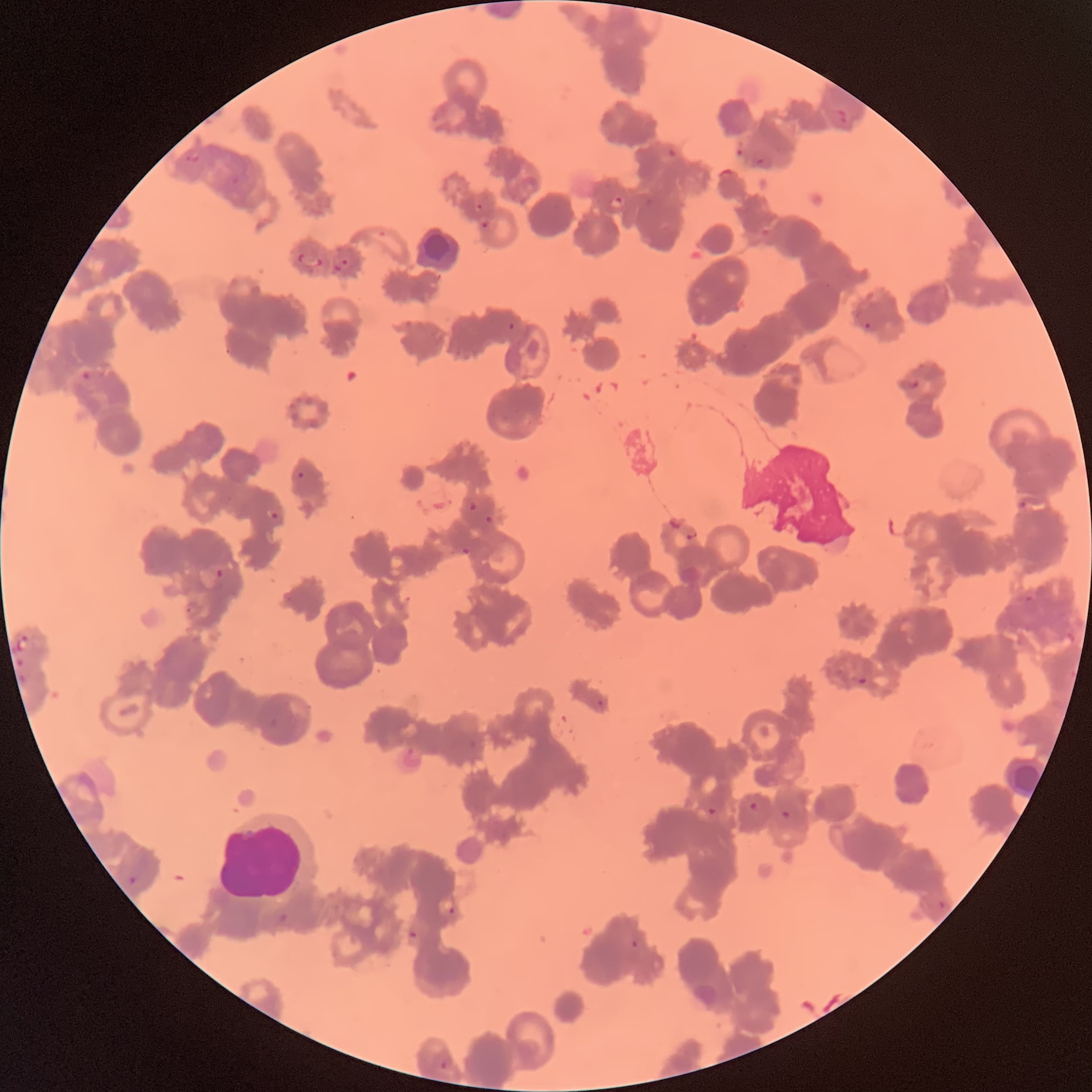
Approximate bounding boxes as named x1/y1/x2/y2 corners in pixels. White blood cell locations: (x1=221, y1=810, x2=302, y2=898). Plasmodium parasite locations: (x1=836, y1=107, x2=849, y2=124), (x1=184, y1=154, x2=200, y2=162), (x1=755, y1=155, x2=772, y2=167), (x1=614, y1=196, x2=625, y2=205), (x1=481, y1=222, x2=489, y2=229), (x1=298, y1=254, x2=324, y2=267), (x1=333, y1=259, x2=348, y2=272), (x1=508, y1=320, x2=515, y2=332), (x1=860, y1=320, x2=873, y2=330), (x1=80, y1=370, x2=91, y2=380), (x1=902, y1=378, x2=919, y2=389), (x1=296, y1=471, x2=305, y2=480), (x1=469, y1=501, x2=478, y2=510), (x1=1018, y1=502, x2=1026, y2=509), (x1=270, y1=512, x2=279, y2=519), (x1=484, y1=516, x2=495, y2=525), (x1=684, y1=527, x2=700, y2=540), (x1=461, y1=547, x2=471, y2=555), (x1=214, y1=568, x2=225, y2=580), (x1=1023, y1=595, x2=1041, y2=614), (x1=185, y1=605, x2=199, y2=615), (x1=15, y1=635, x2=30, y2=651), (x1=16, y1=659, x2=27, y2=684), (x1=858, y1=678, x2=867, y2=684), (x1=597, y1=699, x2=605, y2=707), (x1=748, y1=801, x2=761, y2=812), (x1=708, y1=806, x2=716, y2=816), (x1=781, y1=810, x2=792, y2=819), (x1=130, y1=874, x2=142, y2=884), (x1=437, y1=898, x2=458, y2=916), (x1=939, y1=900, x2=948, y2=909), (x1=409, y1=930, x2=417, y2=938), (x1=631, y1=940, x2=639, y2=948), (x1=439, y1=1058, x2=453, y2=1070). Image is 1092×1092 pixels. The red blood cells show rouleaux formation. Thin blood smear. Optical microscopy.